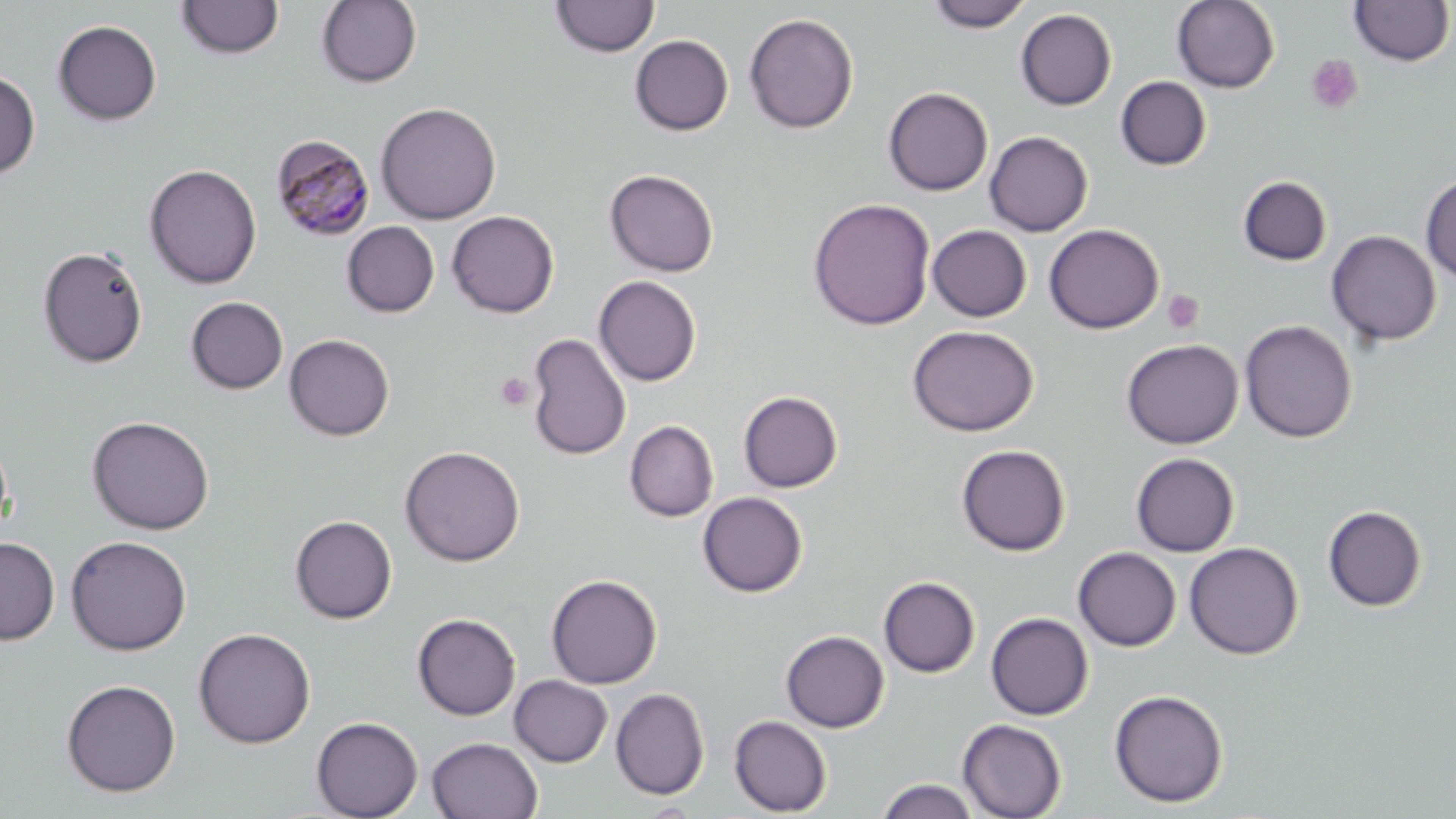
Summary:
  - Coordinate format: approximate bounding boxes as (x1,y1)-(x2,y2) corner pairs in pixels
  - Plasmodium malariae-infected red blood cell locations: (270,134)-(375,240)
  - Uninfected red blood cell locations: (176,0)-(284,60), (316,0)-(421,88), (550,0)-(660,58), (925,0)-(1034,32), (1171,0)-(1280,93), (1348,0)-(1454,67), (1015,9)-(1117,110), (743,13)-(859,134), (52,20)-(162,125), (630,34)-(733,136), (0,68)-(40,179), (1115,76)-(1212,171), (883,86)-(993,196), (376,101)-(501,224), (984,131)-(1093,236), (144,163)-(262,289), (604,169)-(719,277), (1420,174)-(1456,283), (1238,176)-(1332,265), (808,198)-(936,330), (446,210)-(559,318), (342,221)-(439,317), (1044,224)-(1164,333), (927,225)-(1032,322), (1326,230)-(1441,347), (38,244)-(148,369), (594,276)-(701,387), (185,296)-(288,394), (1240,320)-(1357,442), (907,325)-(1039,436), (526,332)-(631,461), (284,334)-(395,440), (1121,338)-(1243,449), (738,391)-(843,493), (87,415)-(215,535), (624,420)-(718,521), (956,444)-(1071,556), (399,445)-(525,566), (1130,452)-(1240,557), (697,492)-(807,597), (1322,505)-(1427,612), (289,515)-(397,624), (65,535)-(192,655), (0,536)-(59,645), (1184,542)-(1303,660), (1073,547)-(1180,651), (546,573)-(662,689), (878,576)-(980,678), (986,612)-(1093,720), (412,613)-(520,720), (193,627)-(315,748), (781,630)-(889,732), (509,675)-(612,767), (61,679)-(181,797), (610,687)-(709,800), (1109,689)-(1228,808), (729,715)-(832,816), (311,716)-(423,819), (957,718)-(1067,819), (427,737)-(543,819), (876,778)-(979,819)
  - Platelet locations: (1306,54)-(1364,114), (1162,290)-(1204,334), (495,372)-(534,411)
  - Slide-level diagnosis: Plasmodium malariae
  - Stain: May-Grünwald-Giemsa
  - Modality: optical microscopy
  - Preparation: thin blood film
  - Image size: 1456×819 pixels
  - Magnification: 1000x
  - Field of view: one of a larger specimen